Locate every Plasmodium parasite.
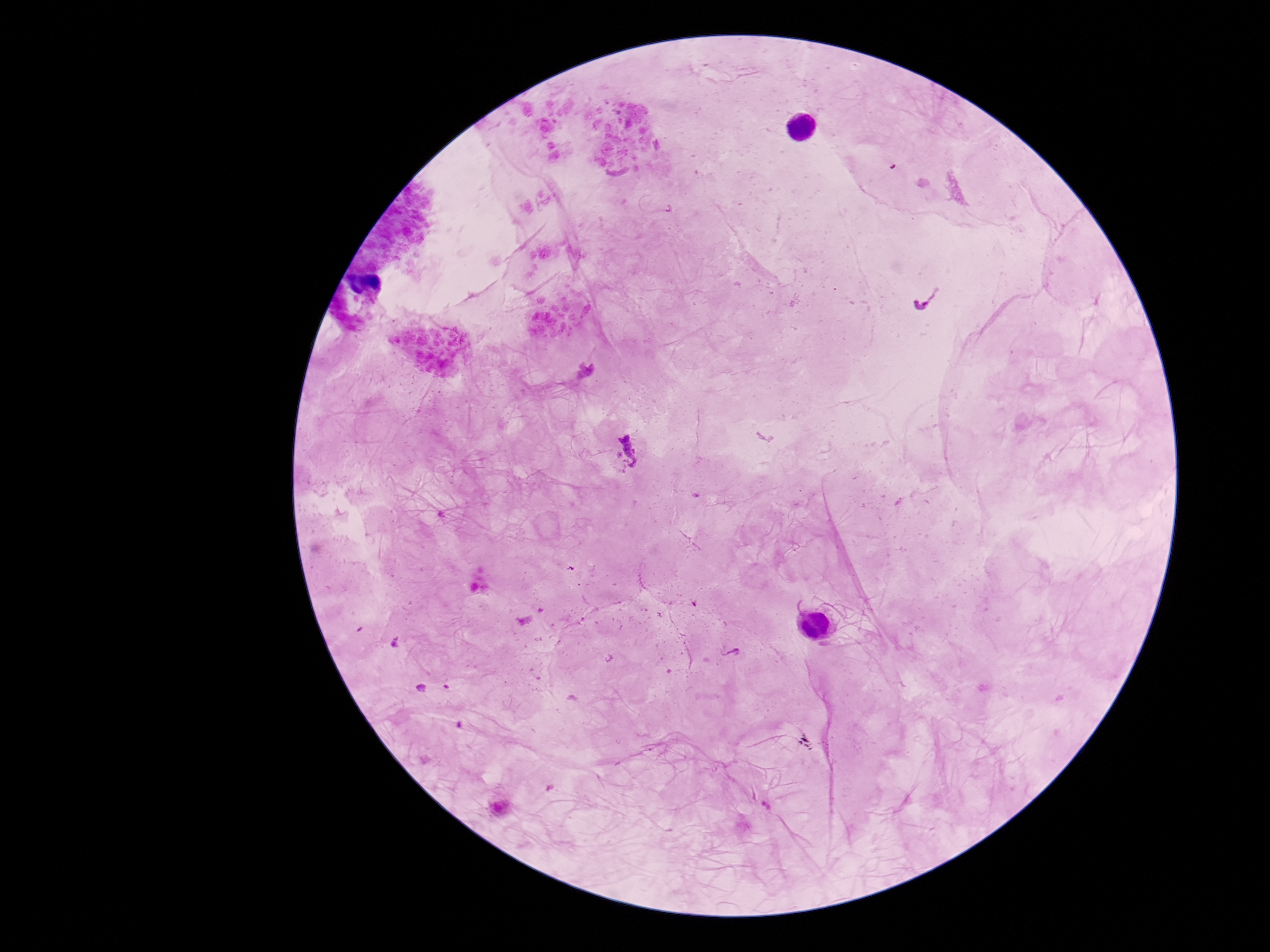

Approximate object centers, in pixels from the top-left corner.
Plasmodium parasites: (x=626, y=451).

magnification: 100x
patient_malaria_status: positive
capture: smartphone camera through the microscope eyepiece
preparation: thick peripheral-blood smear
image_size: 1270×952 pixels
stain: Giemsa
field_of_view: one from this slide